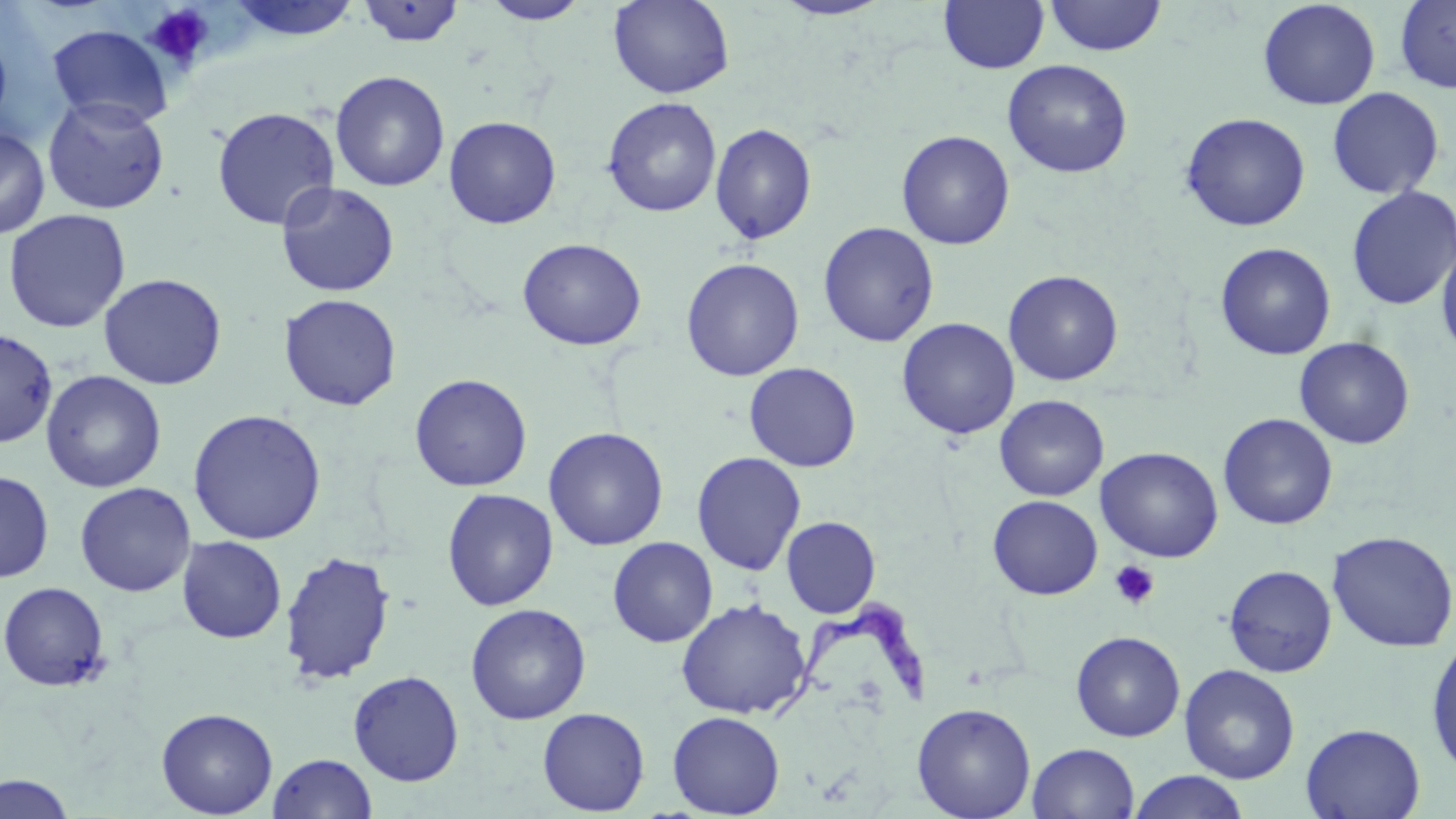
Summary:
  - Coordinate format: approximate bounding boxes as [x1, y1, x2, y2] in pixels
  - Uninfected red blood cell locations: [227, 0, 362, 44], [608, 0, 734, 99], [938, 0, 1050, 74], [1043, 0, 1167, 57], [1257, 0, 1381, 110], [1394, 0, 1456, 94], [355, 1, 466, 48], [481, 1, 590, 25], [771, 1, 894, 21], [46, 24, 173, 129], [0, 32, 12, 131], [1002, 59, 1133, 178], [330, 70, 450, 192], [1327, 87, 1444, 199], [42, 95, 170, 215], [602, 97, 722, 218], [211, 106, 340, 230], [1180, 112, 1310, 232], [443, 116, 561, 229], [709, 123, 817, 245], [0, 126, 50, 239], [897, 130, 1015, 250], [276, 181, 400, 297], [1346, 185, 1456, 310], [3, 209, 131, 333], [818, 221, 939, 348], [517, 238, 647, 351], [1436, 240, 1456, 361], [1215, 242, 1336, 360], [680, 257, 804, 381], [1003, 269, 1123, 386], [99, 273, 227, 390], [279, 293, 402, 411], [897, 317, 1020, 439], [0, 329, 58, 448], [1294, 337, 1414, 449], [744, 362, 861, 472], [41, 370, 167, 493], [409, 373, 532, 492], [994, 394, 1108, 502], [187, 408, 327, 545], [1218, 412, 1338, 530], [543, 427, 669, 551], [1095, 446, 1224, 563], [691, 451, 806, 576], [0, 470, 54, 583], [74, 482, 196, 597], [442, 488, 559, 611], [987, 495, 1103, 600], [781, 516, 881, 618], [1328, 530, 1456, 652], [176, 535, 287, 643], [607, 536, 718, 647], [279, 550, 396, 685], [1223, 564, 1337, 677], [0, 581, 111, 691], [676, 598, 812, 719], [465, 603, 591, 725], [1070, 631, 1185, 741], [1426, 637, 1456, 776], [1179, 664, 1300, 784], [348, 670, 464, 786], [912, 702, 1036, 819], [156, 707, 278, 818], [537, 707, 650, 816], [667, 710, 785, 817], [1300, 723, 1425, 819], [1028, 743, 1139, 819], [269, 752, 377, 819], [1127, 771, 1250, 819], [0, 773, 76, 818]
  - Platelet locations: [144, 4, 215, 69], [1110, 560, 1160, 609]
  - Trypanosoma brucei locations: [759, 596, 933, 724]
  - Slide-level diagnosis: Trypanosoma brucei
  - Field of view: one of a larger specimen
  - Modality: light microscopy
  - Stain: May-Grünwald-Giemsa
  - Image size: 1456×819 pixels
  - Preparation: thin blood film
  - Magnification: 1000x